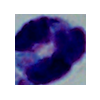
Summary:
  - Modality: photomicrograph
  - Identification: white blood cell
  - Magnification: 1000x